Assess the morphology of the erythrocytes.
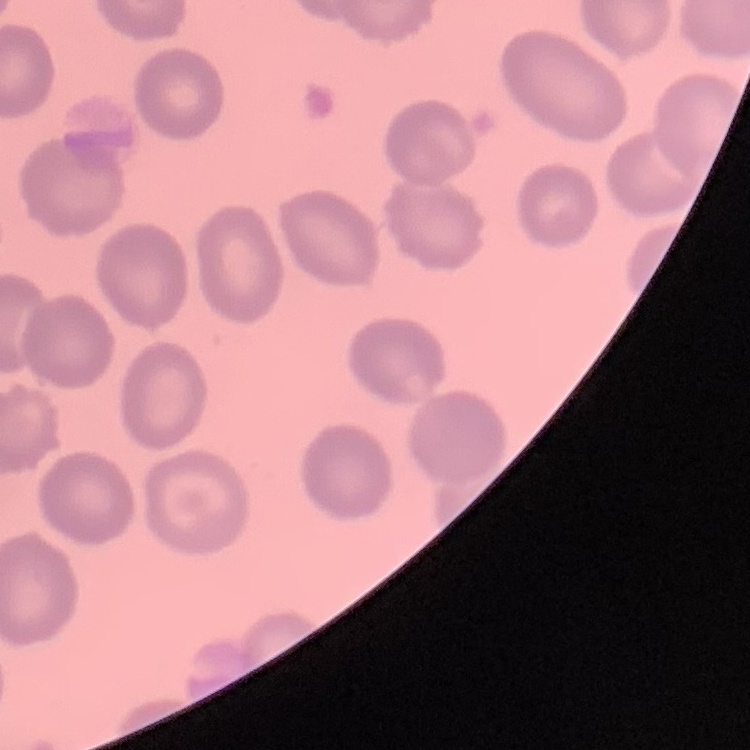

They show no rouleaux formation.

Stained with either Field's or Giemsa. Thin blood smear. Square crop of a larger photomicrograph.